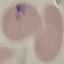
Malaria status: parasitized. Cell patch, automatically extracted from a larger field of view and resized to 64 × 64 pixels. Thin smear of blood. Acquired by smartphone through the microscope eyepiece. Giemsa-stained preparation.